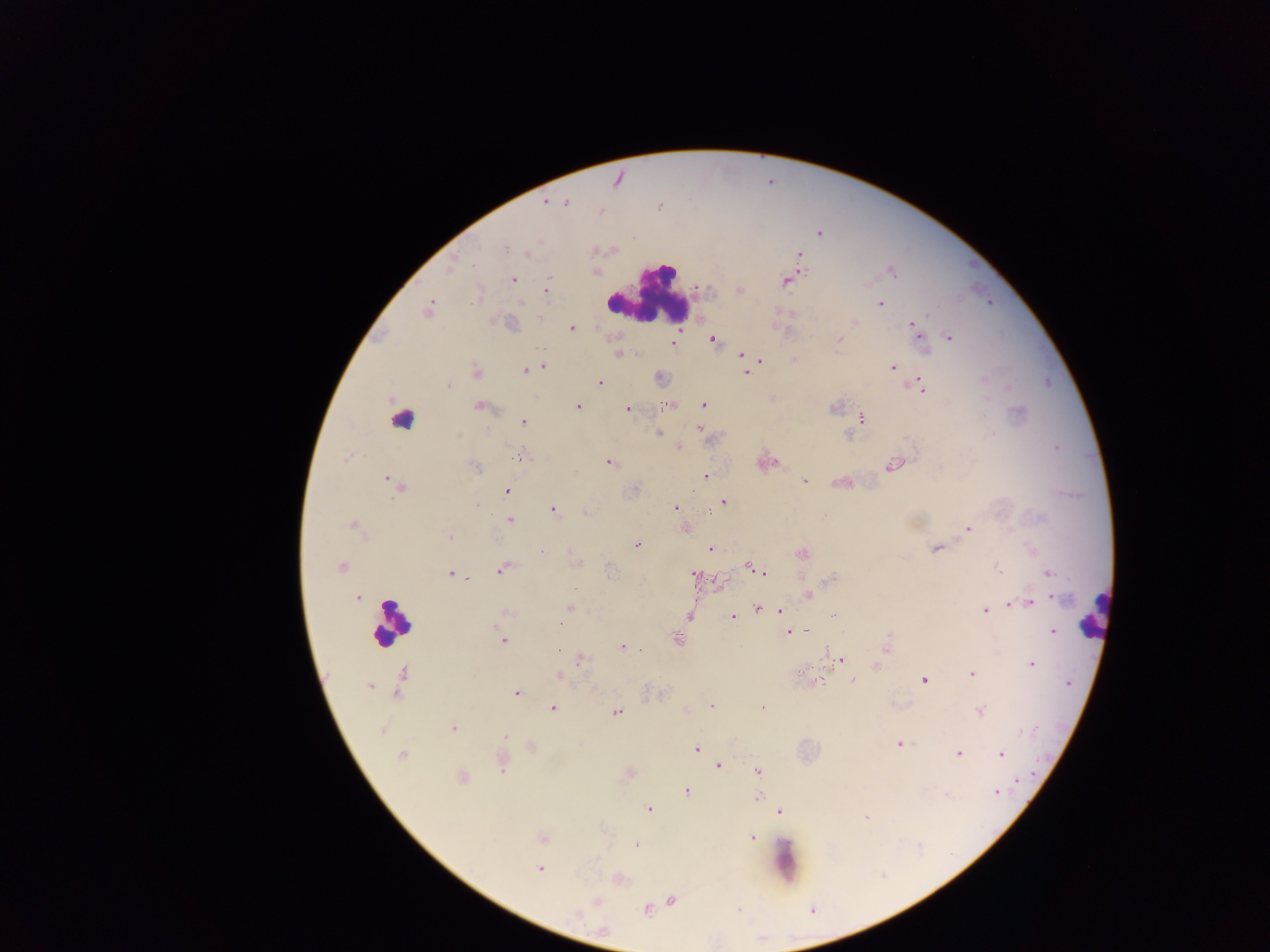

capture = mobile-phone photograph through a microscope
image size = 1270×952 pixels
preparation = thick blood film
Plasmodium parasite locations = approximate centers as (x, y) in pixels: (617, 179), (545, 202), (566, 203), (601, 211), (819, 233), (526, 254), (798, 255), (452, 262), (892, 271), (596, 272), (513, 279), (787, 280), (546, 290), (740, 291), (880, 304), (427, 309), (538, 318), (853, 321), (912, 323), (572, 328), (916, 334), (948, 337), (712, 339), (839, 339), (672, 343), (618, 353), (741, 353), (758, 359), (793, 360), (544, 366), (892, 367), (532, 369), (526, 370), (477, 371), (747, 371), (660, 378), (983, 378), (599, 382), (447, 385), (922, 385), (773, 399), (671, 404), (703, 405), (478, 406), (576, 406), (627, 408), (861, 418), (523, 422), (700, 428), (659, 433), (678, 447), (348, 457), (521, 457), (609, 462), (765, 463), (894, 464), (476, 467), (705, 476), (388, 481), (804, 481), (841, 482), (397, 485), (506, 490), (723, 502), (676, 508), (552, 509), (585, 511), (509, 519), (353, 525), (685, 527), (967, 528), (448, 536), (637, 544), (709, 549), (936, 549), (542, 552), (802, 554), (575, 562), (997, 566), (341, 567), (749, 567), (501, 569), (450, 573), (766, 574), (1047, 574), (694, 577), (718, 582), (808, 594), (358, 597), (1054, 598), (1029, 602), (1009, 605), (568, 608), (757, 608), (780, 610), (985, 610), (505, 613), (732, 615), (688, 616), (1052, 630), (789, 631), (501, 638), (677, 640), (886, 645), (622, 647), (580, 657), (840, 660), (1030, 663), (876, 666), (971, 674), (558, 675), (401, 679), (852, 679), (924, 680), (814, 682), (369, 687), (397, 690), (515, 692), (711, 706), (552, 708), (763, 708), (686, 711), (980, 711), (616, 712), (453, 728), (898, 744), (532, 747), (695, 749), (958, 753), (1001, 754), (401, 755), (501, 763), (717, 765), (757, 772), (628, 773), (461, 777), (686, 790), (995, 792), (758, 797), (648, 809), (778, 811), (866, 818), (751, 836), (542, 837), (636, 845), (539, 868), (617, 879), (670, 900), (597, 901), (647, 909), (576, 913)
leukocyte locations = approximate centers as (x, y) in pixels: (649, 291), (401, 418), (1094, 614), (391, 623), (785, 860)
country = Ghana
field of view = single